Locate every blood parasite and identify its species.
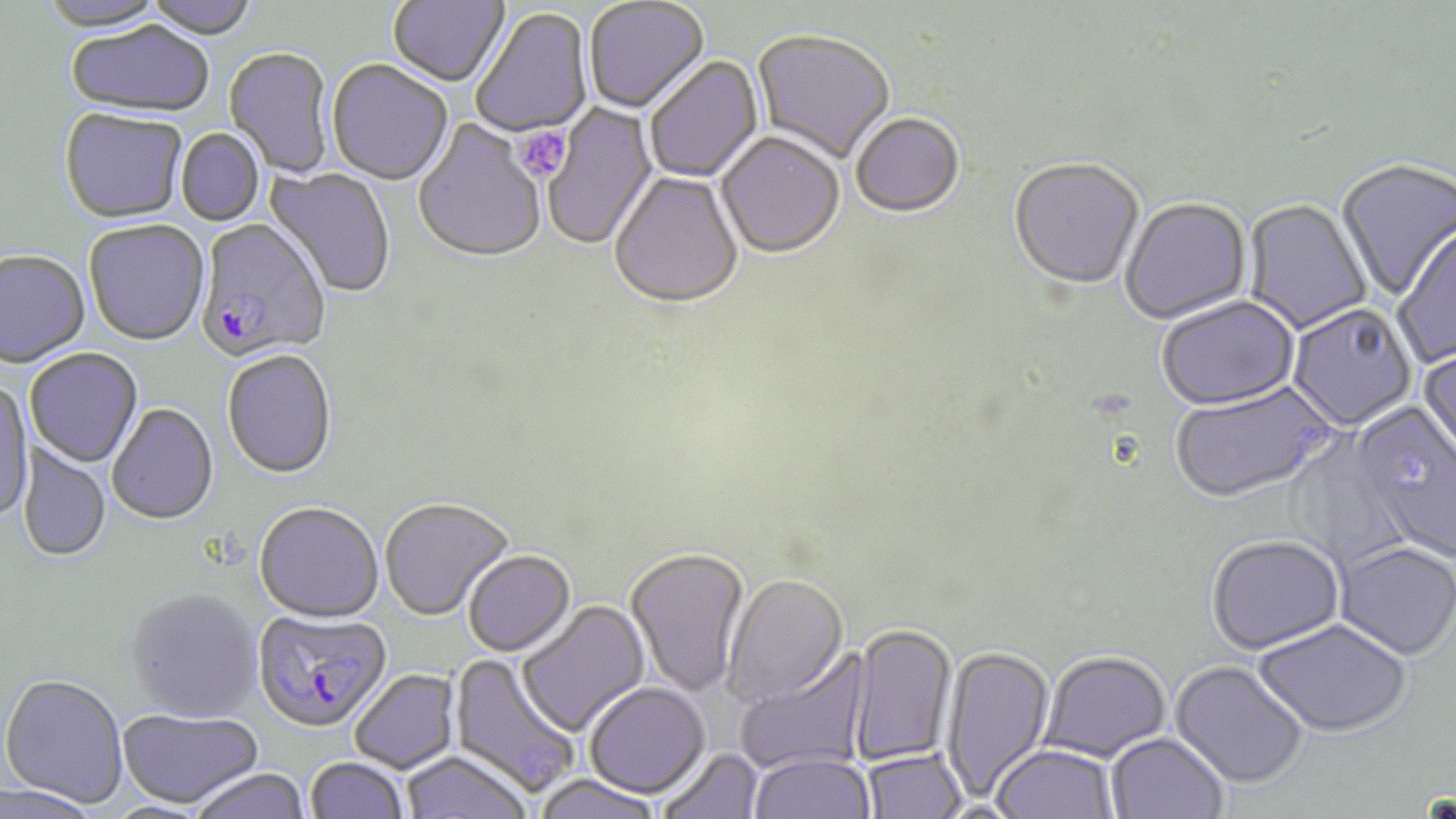
Approximate bounding boxes as [x1, y1, x2, y2] in pixels.
Plasmodium falciparum-infected red blood cells: [196, 220, 331, 364], [253, 609, 392, 734].
No Plasmodium ovale, Plasmodium malariae, Plasmodium vivax, Babesia divergens, or Trypanosoma brucei observed.

Summary:
  - Uninfected red blood cell locations: [40, 0, 170, 35], [143, 0, 261, 42], [387, 0, 510, 89], [584, 0, 710, 115], [472, 8, 594, 139], [66, 24, 214, 121], [751, 31, 895, 166], [223, 49, 335, 179], [644, 56, 764, 183], [327, 61, 453, 187], [541, 102, 659, 253], [59, 110, 188, 226], [851, 115, 965, 220], [412, 120, 546, 267], [176, 129, 264, 227], [716, 133, 845, 261], [1007, 160, 1145, 293], [1335, 160, 1456, 303], [262, 164, 396, 300], [609, 172, 744, 313], [1119, 199, 1252, 326], [1242, 200, 1373, 335], [84, 221, 209, 348], [1393, 226, 1456, 369], [0, 252, 90, 370], [1156, 298, 1300, 413], [1287, 304, 1417, 432], [1417, 344, 1456, 478], [25, 348, 144, 469], [221, 351, 337, 481], [0, 379, 33, 523], [1169, 382, 1338, 506], [107, 404, 218, 527], [1354, 408, 1456, 562], [1285, 436, 1412, 569], [18, 442, 111, 563], [380, 498, 515, 623], [254, 504, 384, 625], [1206, 537, 1345, 658], [1333, 544, 1456, 663], [625, 548, 751, 698], [463, 551, 577, 658], [722, 574, 848, 708], [126, 589, 262, 722], [516, 600, 652, 739], [1253, 621, 1411, 740], [847, 625, 957, 767], [940, 644, 1055, 804], [734, 648, 871, 774], [448, 652, 581, 799], [1040, 653, 1172, 764], [1169, 662, 1308, 791], [349, 670, 461, 775], [1, 673, 128, 809], [584, 682, 710, 799], [116, 708, 263, 809], [1105, 733, 1228, 819], [992, 746, 1118, 819], [659, 747, 763, 819], [862, 748, 967, 819], [400, 750, 534, 819], [749, 752, 875, 819], [305, 757, 409, 818], [187, 769, 311, 819], [531, 775, 664, 819], [0, 781, 101, 819]
  - Platelet locations: [515, 126, 572, 182]
  - Slide-level diagnosis: Plasmodium falciparum
  - Image size: 1456×819 pixels
  - Field of view: one of a larger specimen
  - Stain: May-Grünwald-Giemsa
  - Preparation: thin blood smear
  - Magnification: 1000x
  - Modality: optical microscopy